Report the malaria status of this cell.
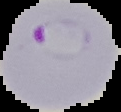

It is parasitized.

image size = 121×112 pixels
image type = cell region segmented out of the field of view; surrounding area masked to black
preparation = thin blood film